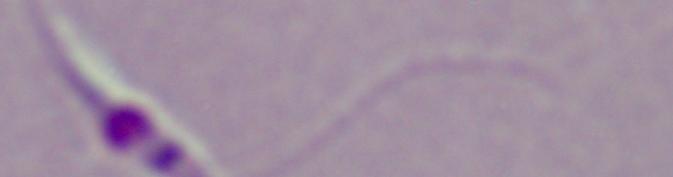

modality = micrograph
identification = Leishmania
magnification = 1000x